Comment on the morphology of the red blood cells.
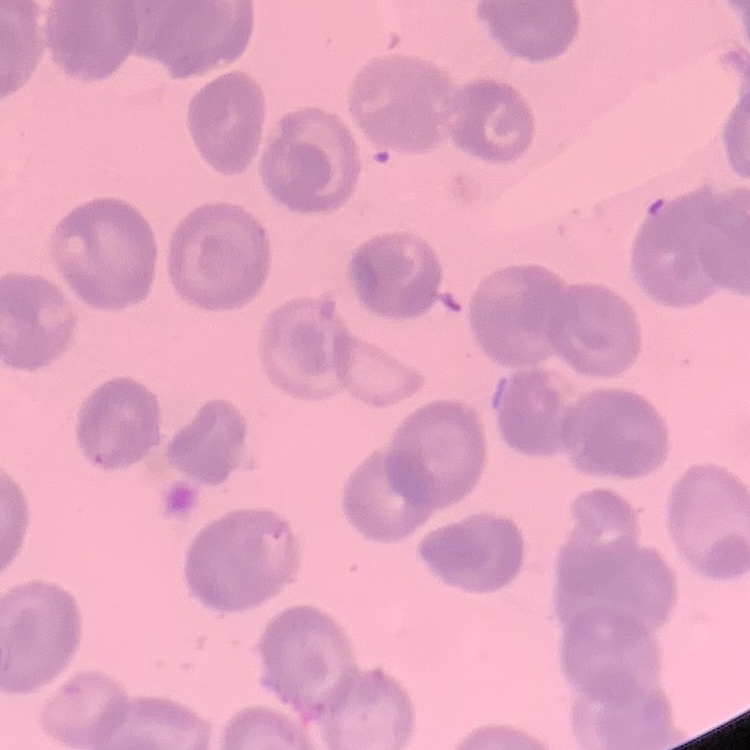
They show no rouleaux formation.

Summary:
  - Preparation: thin blood smear
  - Stain: Field's or Giemsa
  - Image type: square crop of a larger photomicrograph